Report the malaria status of this cell.
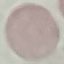
Uninfected.

Summary:
  - Image type: cell patch, automatically extracted from a larger field of view and resized to 64 × 64 pixels
  - Capture: smartphone camera at the microscope eyepiece
  - Preparation: thin smear
  - Stain: Giemsa